Locate every Plasmodium vivax-infected red blood cell.
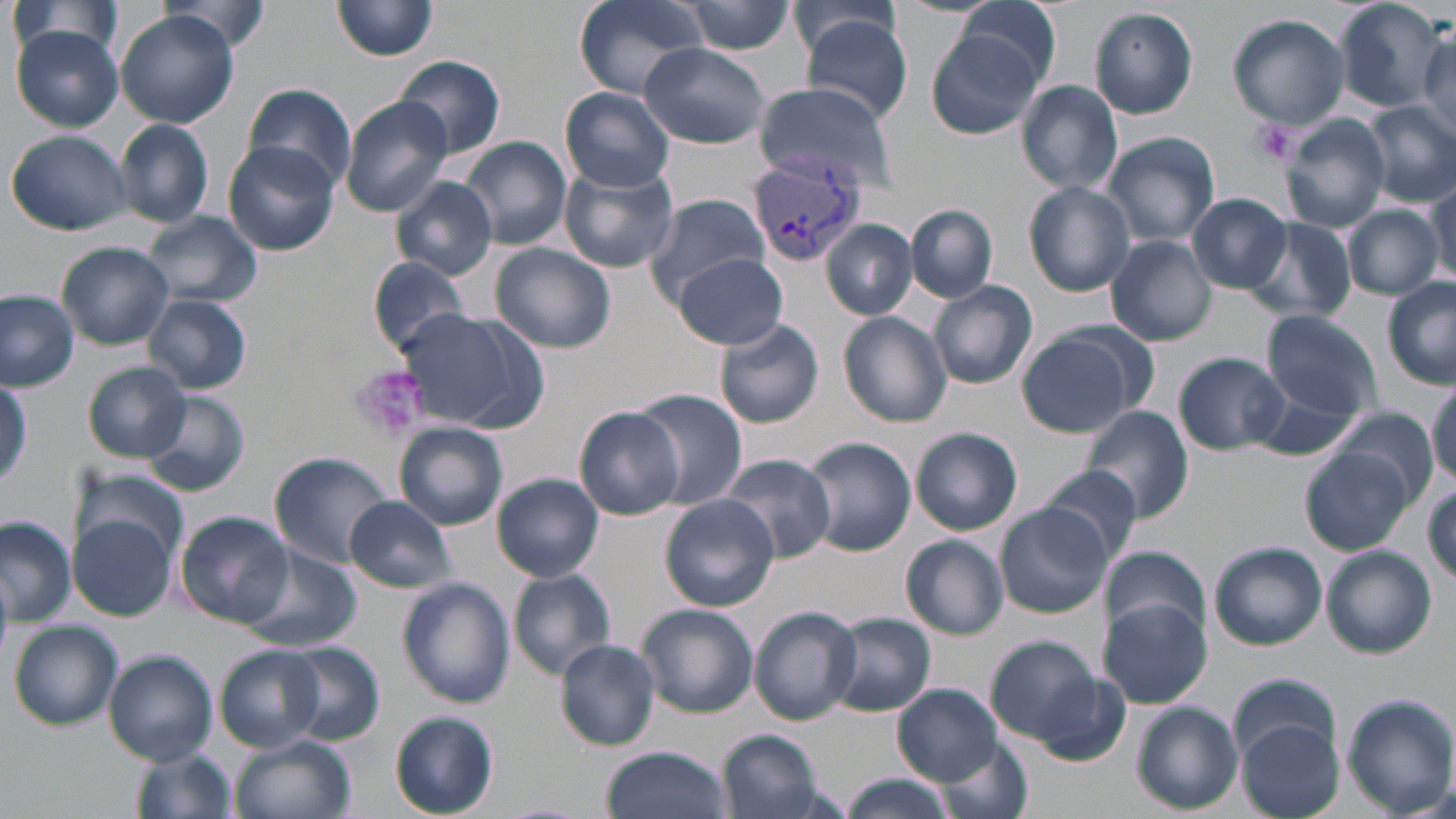
Approximate bounding boxes as (x1, y1, x2, y2) in pixels.
Plasmodium vivax-infected red blood cells: (747, 157, 868, 268).

Summary:
  - Platelet locations: (1249, 118, 1298, 166), (348, 363, 430, 440)
  - Uninfected red blood cell locations: (333, 0, 439, 60), (574, 0, 708, 98), (1332, 0, 1449, 113), (158, 1, 273, 59), (956, 1, 1063, 88), (5, 2, 125, 67), (683, 2, 798, 54), (789, 3, 905, 70), (1090, 7, 1199, 120), (116, 11, 237, 129), (1227, 13, 1352, 130), (802, 17, 913, 123), (10, 25, 124, 131), (926, 27, 1044, 138), (1417, 27, 1454, 138), (639, 43, 770, 148), (393, 55, 505, 160), (1017, 80, 1124, 196), (242, 81, 358, 193), (755, 82, 897, 188), (562, 88, 674, 192), (340, 97, 452, 216), (1363, 101, 1456, 207), (1281, 115, 1390, 232), (114, 119, 214, 229), (7, 129, 132, 235), (1101, 132, 1220, 248), (459, 135, 570, 250), (223, 142, 340, 258), (559, 162, 679, 272), (389, 174, 498, 281), (1024, 181, 1136, 296), (1425, 184, 1456, 285), (646, 192, 769, 302), (1188, 193, 1292, 293), (907, 203, 997, 303), (1344, 205, 1444, 301), (143, 213, 262, 307), (1245, 218, 1357, 324), (823, 220, 917, 322), (1106, 236, 1216, 346), (490, 242, 619, 353), (58, 243, 174, 349), (676, 254, 790, 349), (368, 255, 476, 359), (1383, 278, 1456, 388), (929, 279, 1038, 392), (0, 289, 79, 392), (143, 293, 252, 395), (393, 306, 537, 431), (1261, 309, 1384, 417), (838, 311, 952, 428), (713, 319, 825, 430), (1016, 326, 1147, 438), (1174, 352, 1288, 455), (82, 363, 190, 463), (0, 375, 30, 491), (1428, 376, 1456, 485), (1241, 383, 1364, 461), (636, 391, 748, 508), (142, 392, 251, 497), (1327, 406, 1439, 509), (575, 407, 687, 521), (1081, 407, 1191, 528), (394, 422, 508, 530), (911, 428, 1023, 536), (802, 436, 916, 557), (1302, 445, 1416, 555), (270, 449, 393, 568), (718, 452, 836, 563), (1039, 466, 1145, 564), (74, 467, 189, 560), (491, 474, 604, 583), (344, 495, 456, 593), (659, 496, 778, 612), (994, 504, 1111, 619), (174, 511, 294, 628), (71, 514, 177, 619), (0, 516, 75, 626), (900, 535, 1009, 640), (1209, 541, 1327, 650), (1322, 546, 1436, 657), (243, 547, 361, 655), (1102, 548, 1211, 639), (509, 570, 618, 680), (397, 577, 515, 709), (1096, 599, 1213, 709), (637, 604, 757, 718), (749, 606, 862, 725), (830, 613, 937, 717), (10, 620, 124, 730), (986, 635, 1104, 746), (554, 638, 662, 751), (280, 642, 385, 745), (216, 647, 327, 752), (103, 650, 217, 767), (1025, 667, 1131, 764), (1229, 674, 1340, 767), (892, 683, 1002, 784), (1343, 694, 1456, 816), (1134, 700, 1243, 815), (389, 710, 500, 818), (1239, 722, 1345, 818), (718, 729, 824, 819), (230, 734, 356, 819), (936, 737, 1035, 819), (601, 745, 731, 819), (131, 747, 237, 819), (836, 774, 960, 819)
  - Slide-level diagnosis: Plasmodium vivax
  - Stain: May-Grünwald-Giemsa
  - Image size: 1456×819 pixels
  - Modality: light microscopy
  - Preparation: thin blood film
  - Field of view: single
  - Magnification: 1000x